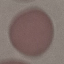

Malaria status: uninfected. Giemsa-stained preparation. Acquired by smartphone through the microscope eyepiece. Cell patch, automatically extracted from a larger field of view and resized to 64 × 64 pixels. Thin blood film.